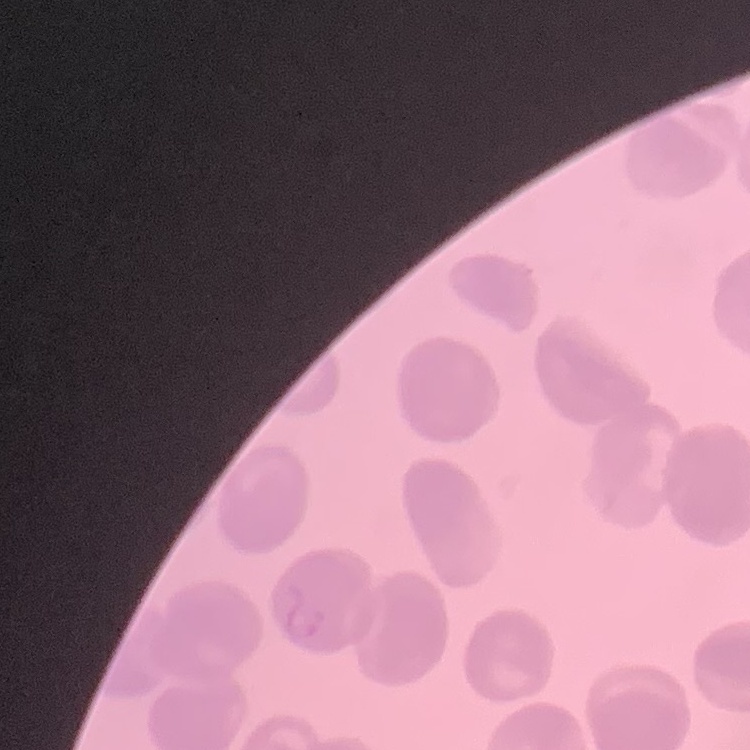

The erythrocytes show no rouleaux formation. Thin peripheral smear. Field's or Giemsa stain. One tile cut from a larger photomicrograph.